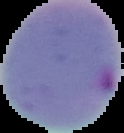
image size = 124×133 pixels
image type = segmented cell region on a black background
preparation = thin blood film
result = Plasmodium parasites identified